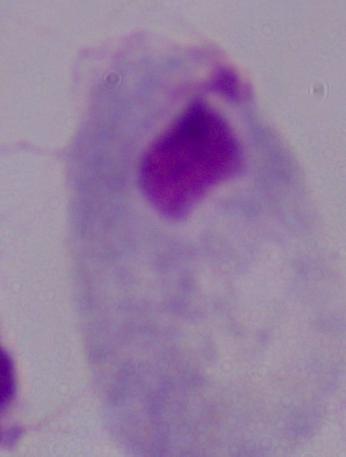
Summary:
  - Magnification: 1000x
  - Identification: trichomonad
  - Modality: micrograph